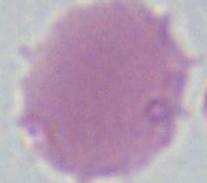
modality: micrograph
identification: red blood cell
magnification: 1000x